Name the parasite shown.
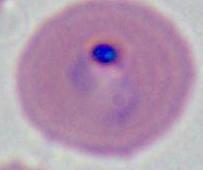

Plasmodium.

Micrograph. Captured at either 400x or 1000x magnification.